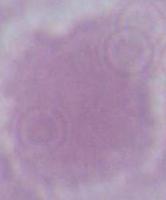

Photomicrograph. Captured at 1000x magnification. A red blood cell is seen.